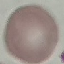 Malaria status: uninfected. Giemsa-stained preparation. Thin blood film. Acquired by smartphone through the microscope eyepiece. Cell patch, automatically extracted from a larger field of view and resized to 64 × 64 pixels.